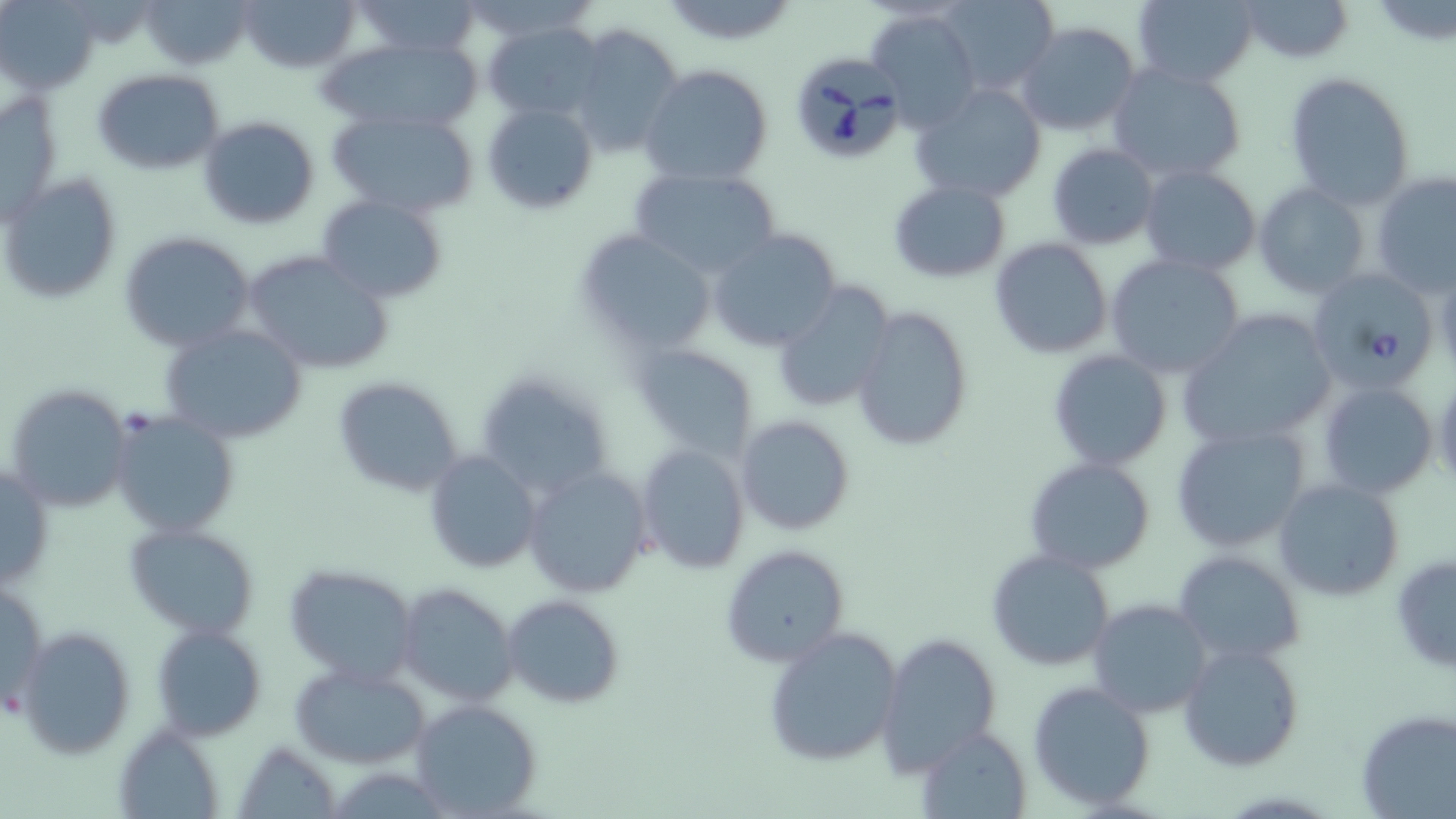
slide_level_diagnosis: Babesia divergens
field_of_view: one of a larger specimen
modality: optical microscopy
magnification: 1000x
uninfected_red_blood_cell_locations: 'approximate bounding boxes as named x1/y1/x2/y2 corners in pixels: (x1=142, y1=0, x2=252, y2=71), (x1=240, y1=0, x2=360, y2=74), (x1=347, y1=0, x2=488, y2=60), (x1=935, y1=0, x2=1061, y2=95), (x1=1130, y1=0, x2=1258, y2=87), (x1=1236, y1=0, x2=1356, y2=64), (x1=3, y1=2, x2=100, y2=95), (x1=868, y1=8, x2=982, y2=131), (x1=481, y1=19, x2=607, y2=122), (x1=1014, y1=21, x2=1142, y2=138), (x1=567, y1=23, x2=684, y2=158), (x1=319, y1=35, x2=487, y2=136), (x1=1106, y1=62, x2=1249, y2=188), (x1=640, y1=63, x2=774, y2=188), (x1=92, y1=68, x2=225, y2=176), (x1=1283, y1=71, x2=1417, y2=208), (x1=909, y1=83, x2=1047, y2=204), (x1=2, y1=89, x2=64, y2=224), (x1=482, y1=101, x2=598, y2=215), (x1=327, y1=106, x2=481, y2=217), (x1=197, y1=115, x2=320, y2=230), (x1=1047, y1=142, x2=1159, y2=249), (x1=1139, y1=164, x2=1262, y2=275), (x1=627, y1=165, x2=783, y2=279), (x1=1, y1=172, x2=122, y2=304), (x1=1372, y1=173, x2=1456, y2=297), (x1=887, y1=178, x2=1012, y2=283), (x1=1252, y1=182, x2=1371, y2=300), (x1=318, y1=195, x2=449, y2=304), (x1=707, y1=228, x2=842, y2=351), (x1=118, y1=230, x2=257, y2=352), (x1=574, y1=231, x2=716, y2=356), (x1=989, y1=236, x2=1114, y2=360), (x1=243, y1=251, x2=393, y2=375), (x1=1105, y1=252, x2=1247, y2=380), (x1=768, y1=281, x2=895, y2=414), (x1=849, y1=306, x2=975, y2=453), (x1=1176, y1=310, x2=1339, y2=456), (x1=159, y1=321, x2=308, y2=446), (x1=632, y1=340, x2=759, y2=459), (x1=1048, y1=349, x2=1172, y2=471), (x1=473, y1=367, x2=616, y2=503), (x1=333, y1=376, x2=466, y2=499), (x1=1317, y1=381, x2=1439, y2=500), (x1=4, y1=383, x2=134, y2=513), (x1=110, y1=410, x2=240, y2=538), (x1=735, y1=415, x2=855, y2=535), (x1=1172, y1=423, x2=1311, y2=553), (x1=636, y1=443, x2=750, y2=574), (x1=424, y1=449, x2=542, y2=573), (x1=1024, y1=457, x2=1155, y2=573), (x1=0, y1=462, x2=53, y2=593), (x1=522, y1=464, x2=652, y2=598), (x1=1272, y1=477, x2=1405, y2=603), (x1=124, y1=522, x2=261, y2=638), (x1=721, y1=545, x2=847, y2=667), (x1=985, y1=549, x2=1116, y2=672), (x1=1172, y1=549, x2=1305, y2=668), (x1=1390, y1=553, x2=1455, y2=675), (x1=284, y1=562, x2=420, y2=685), (x1=1, y1=577, x2=48, y2=719), (x1=395, y1=582, x2=516, y2=709), (x1=504, y1=595, x2=624, y2=709), (x1=1089, y1=598, x2=1212, y2=719), (x1=150, y1=623, x2=266, y2=743), (x1=17, y1=627, x2=135, y2=759), (x1=762, y1=627, x2=901, y2=769), (x1=877, y1=632, x2=1002, y2=775), (x1=1177, y1=640, x2=1304, y2=772), (x1=288, y1=660, x2=432, y2=769), (x1=1027, y1=680, x2=1156, y2=810), (x1=409, y1=699, x2=543, y2=816), (x1=1356, y1=708, x2=1453, y2=818), (x1=115, y1=725, x2=224, y2=818), (x1=915, y1=725, x2=1033, y2=818), (x1=235, y1=741, x2=341, y2=817)'
babesia_divergens_infected_red_blood_cell_locations: 'approximate bounding boxes as named x1/y1/x2/y2 corners in pixels: (x1=788, y1=51, x2=910, y2=164), (x1=1314, y1=273, x2=1435, y2=393)'
stain: May-Grünwald-Giemsa
preparation: thin blood film
image_size: 1456×819 pixels